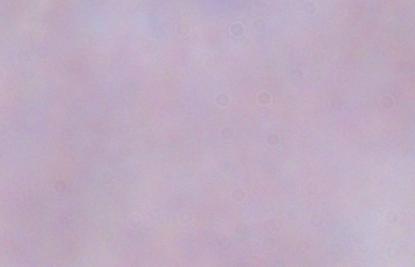

Summary:
  - Identification: trypanosome
  - Magnification: 1000x
  - Modality: photomicrograph